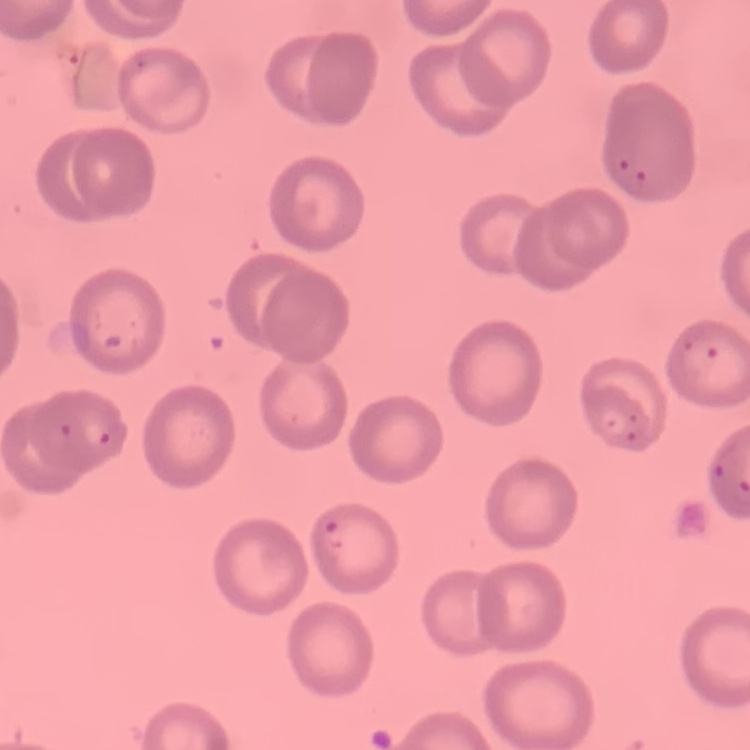

{
  "red_blood_cell_morphology": "no rouleaux formation",
  "preparation": "thin blood film",
  "image_type": "square crop of a larger photomicrograph",
  "stain": "Field's or Giemsa"
}